Classify this cell by malaria status.
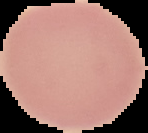

Uninfected.

Image is 148×133 pixels. From a thin blood film. The area outside the segmented cell region is set to black.